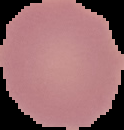

Summary:
  - Image type: segmented cell region with the area outside set to black
  - Malaria status: uninfected
  - Image size: 124×130 pixels
  - Preparation: thin blood smear